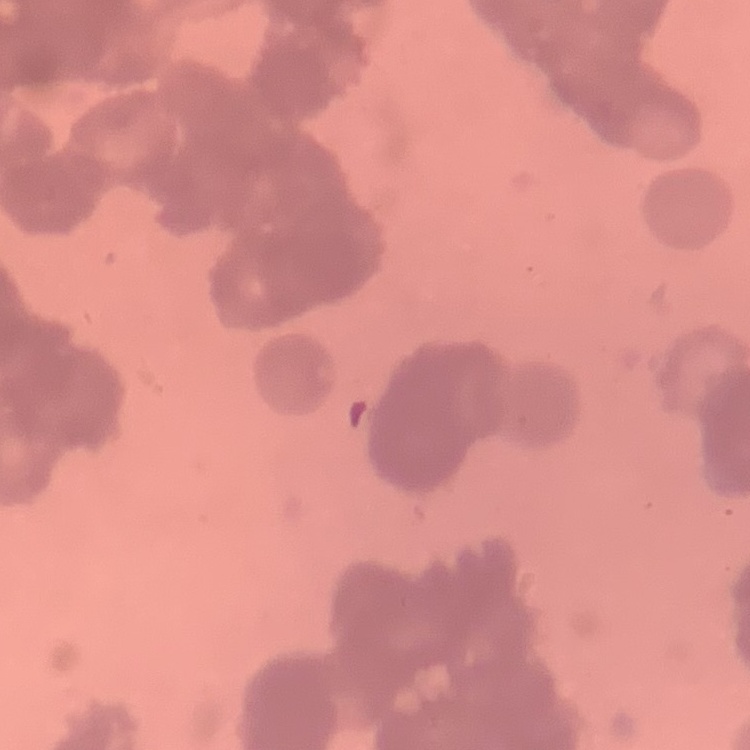
Summary:
  - Erythrocyte morphology: rouleaux formation
  - Preparation: thin blood smear
  - Image type: one tile cut from a larger photomicrograph
  - Stain: Field's or Giemsa